Report the malaria status of this cell.
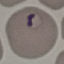

It is parasitized.

Summary:
  - Stain: Giemsa
  - Image type: automatically extracted cell patch, resized to 64 × 64 pixels
  - Preparation: thin blood smear
  - Capture: smartphone through the microscope eyepiece